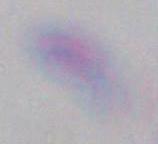

Summary:
  - Magnification: 1000x
  - Identification: Toxoplasma gondii
  - Modality: micrograph